Report the malaria status.
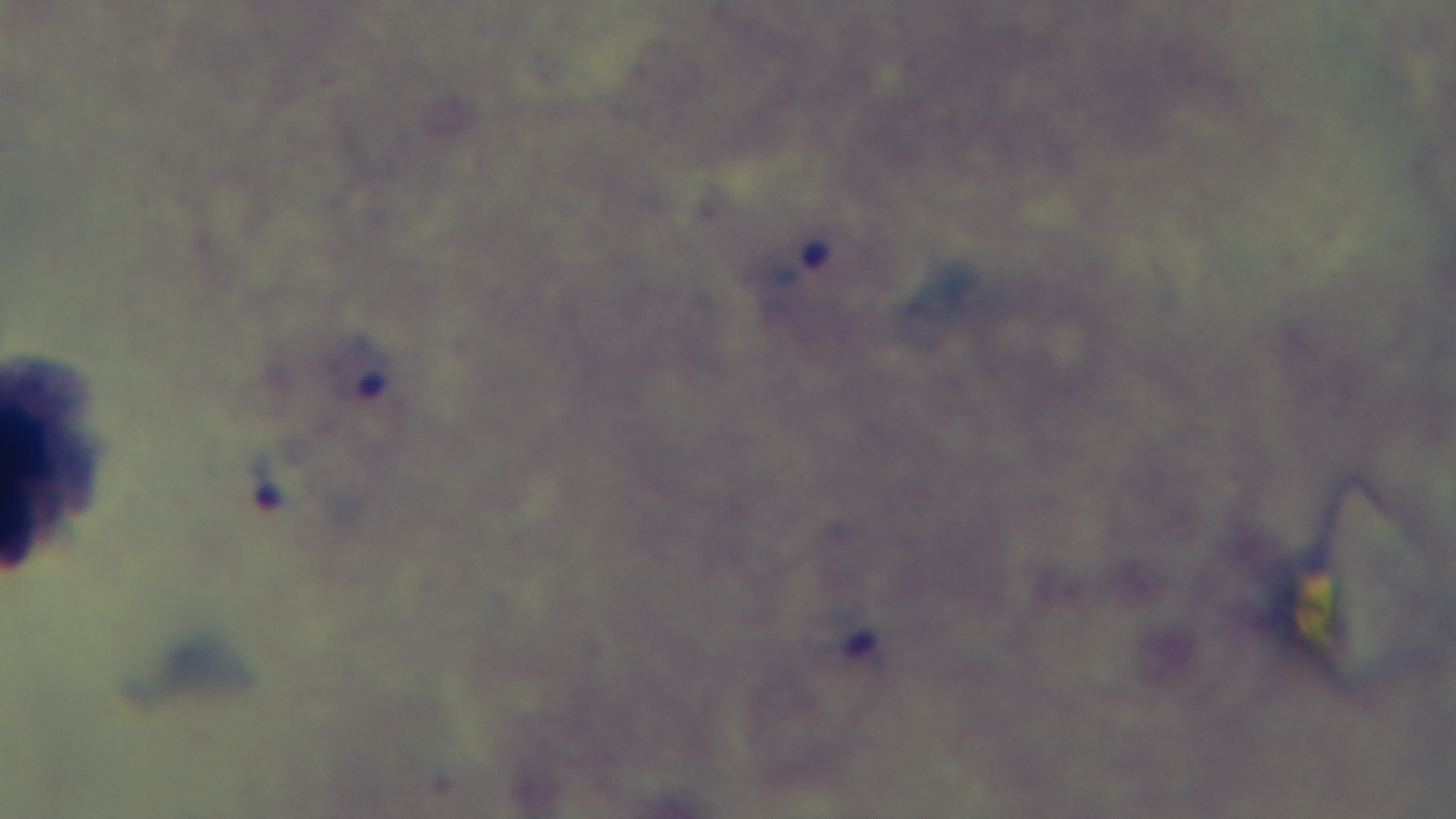

It is infected.

Captured with a mounted 4K digital camera. Giemsa-stained. Preparation: thick blood film. 100x oil-immersion objective. Photomicrograph. One field from the slide.